Report the malaria status of this cell.
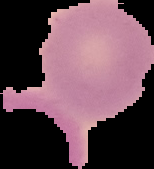
Uninfected.

Image is 154×169 pixels. From a thin blood film. Cell region segmented out of the field of view; the surrounding area is masked to black.